Locate every Plasmodium falciparum parasite and identify its life-cycle stage.
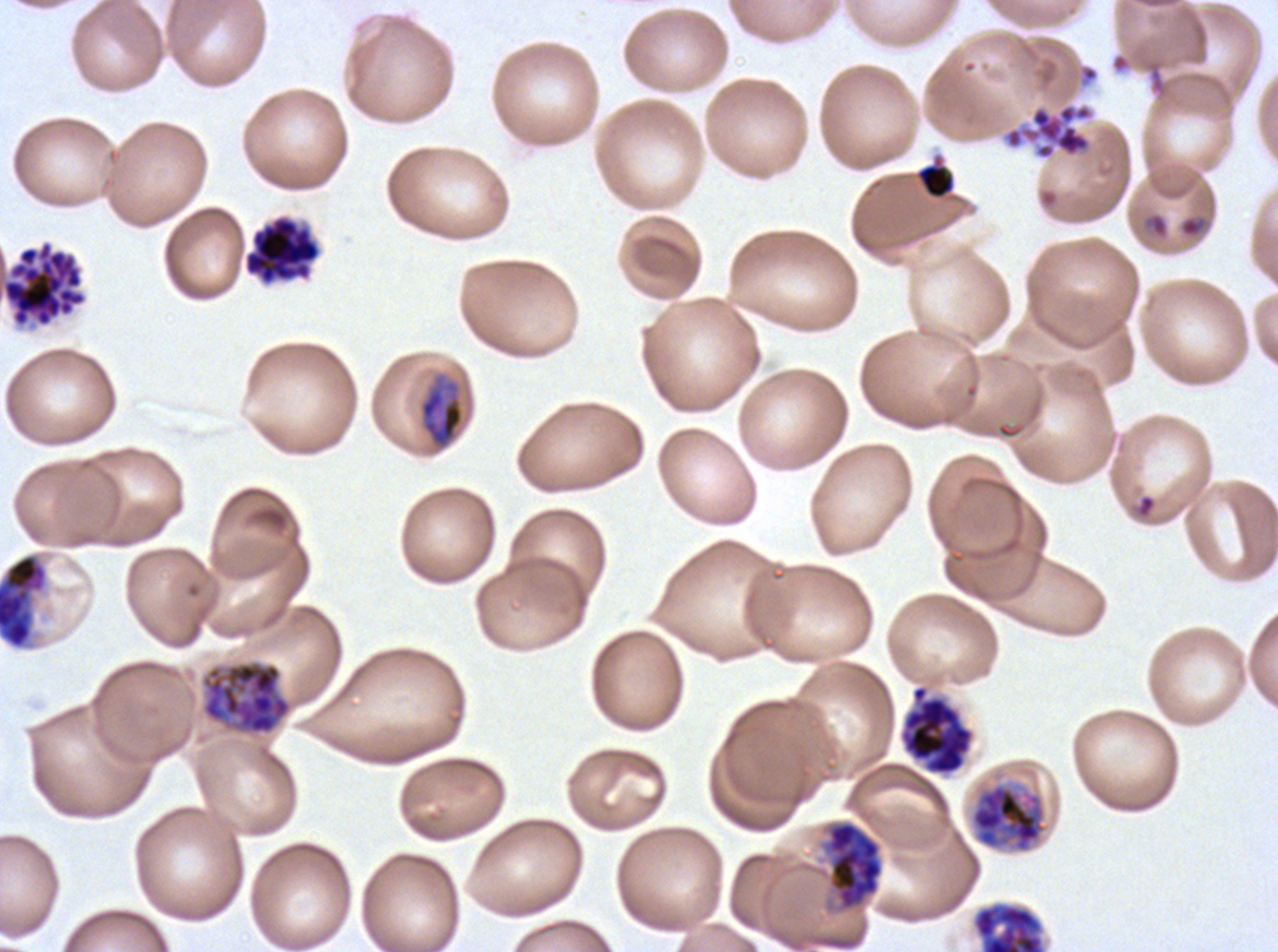
Approximate bounding boxes as {x1, y1, x2, y2} in pixels.
Rings: {1179, 216, 1203, 238}.
Mid trophozoites: {418, 374, 464, 450}.
Early schizonts: {0, 553, 48, 649}, {199, 658, 294, 737}, {969, 781, 1049, 854}, {825, 821, 884, 911}.
Late schizonts: {972, 903, 1044, 951}.
Segmenters: {1004, 103, 1093, 160}, {243, 215, 321, 286}, {1, 240, 87, 327}, {899, 685, 974, 775}.
No late-ring/early-trophozoite forms, late trophozoites, or gametocytes observed.

Summary:
  - Stain: Giemsa
  - Life-cycle stages observed: ring, mid trophozoite, early schizont, late schizont, segmenter
  - Specimen: ex-vivo Plasmodium falciparum culture from a patient in The Gambia, grown for 24 to 48 hours
  - Image size: 1278×952 pixels
  - Preparation: thin blood film
  - Field of view: sub-image separated from a larger composite